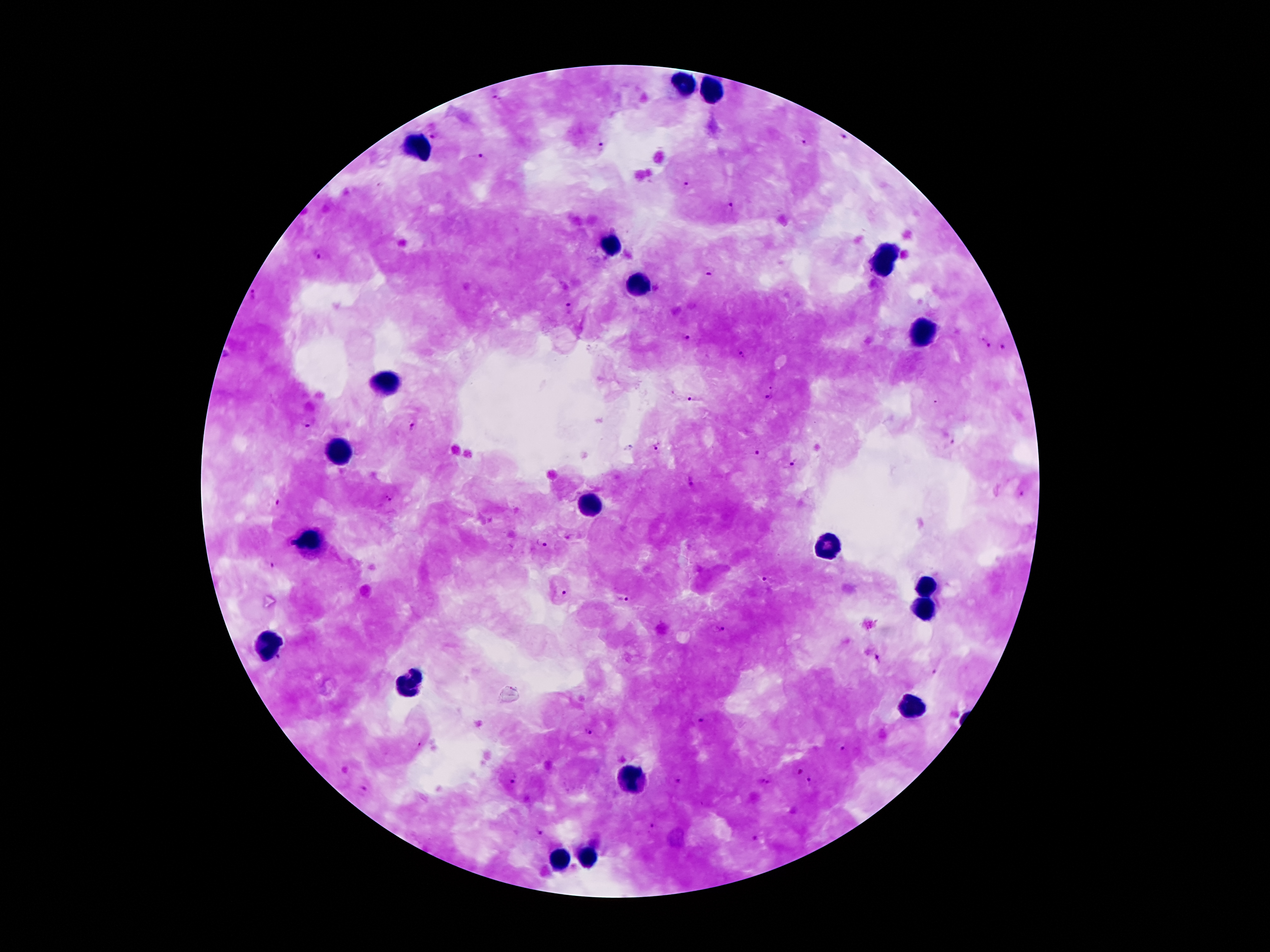 Approximate object centers, in pixels from the top-left corner. Leukocyte locations: (x=684, y=83), (x=711, y=91), (x=425, y=147), (x=611, y=242), (x=881, y=262), (x=638, y=283), (x=919, y=335), (x=389, y=383), (x=336, y=454), (x=591, y=503), (x=311, y=543), (x=824, y=543), (x=926, y=589), (x=924, y=606), (x=271, y=644), (x=412, y=685), (x=912, y=708), (x=632, y=779), (x=588, y=858), (x=561, y=860). Plasmodium parasite locations: (x=497, y=97), (x=434, y=136), (x=844, y=136), (x=804, y=142), (x=602, y=148), (x=482, y=157), (x=687, y=184), (x=731, y=207), (x=319, y=255), (x=710, y=270), (x=568, y=305), (x=684, y=337), (x=986, y=342), (x=1004, y=348), (x=743, y=354), (x=772, y=384), (x=770, y=396), (x=694, y=399), (x=937, y=402), (x=307, y=424), (x=412, y=428), (x=953, y=440), (x=658, y=448), (x=761, y=455), (x=794, y=462), (x=690, y=483), (x=1022, y=494), (x=388, y=498), (x=278, y=503), (x=541, y=543), (x=275, y=563), (x=766, y=581), (x=564, y=593), (x=624, y=600), (x=719, y=629), (x=279, y=658), (x=878, y=659), (x=936, y=670), (x=702, y=720), (x=588, y=731), (x=418, y=745), (x=844, y=751), (x=799, y=770), (x=515, y=779), (x=678, y=782), (x=765, y=782), (x=811, y=783), (x=363, y=789), (x=652, y=824), (x=540, y=834), (x=756, y=838). Patient malaria status: infected with Plasmodium falciparum. Thick peripheral-blood smear. Single field of view. 100x magnification. Image is 1270×952 pixels. Giemsa stain. Smartphone photograph taken through the microscope eyepiece.